Name the parasite shown.
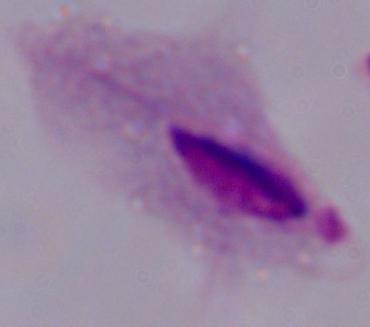

This is a trichomonad.

Summary:
  - Magnification: 1000x
  - Modality: micrograph